Classify this cell by malaria status.
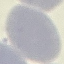
It is uninfected.

{
  "image_type": "cell patch, automatically extracted from a larger field of view and resized to 64 × 64 pixels",
  "stain": "Giemsa",
  "preparation": "thin smear",
  "capture": "smartphone camera at the microscope eyepiece"
}